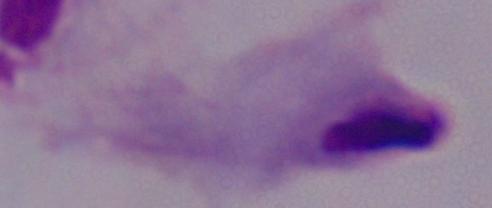
A trichomonad is shown. 1000x magnification. Micrograph.